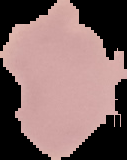

Summary:
  - Image size: 127×160 pixels
  - Image type: segmented cell region with the area outside set to black
  - Malaria status: uninfected
  - Preparation: thin blood smear